Classify this cell by malaria status.
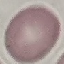
It is uninfected.

Summary:
  - Capture: smartphone camera at the microscope eyepiece
  - Image type: cell patch, automatically extracted from a larger field of view and resized to 64 × 64 pixels
  - Stain: Giemsa
  - Preparation: thin blood film